Locate every blood parasite and identify its species.
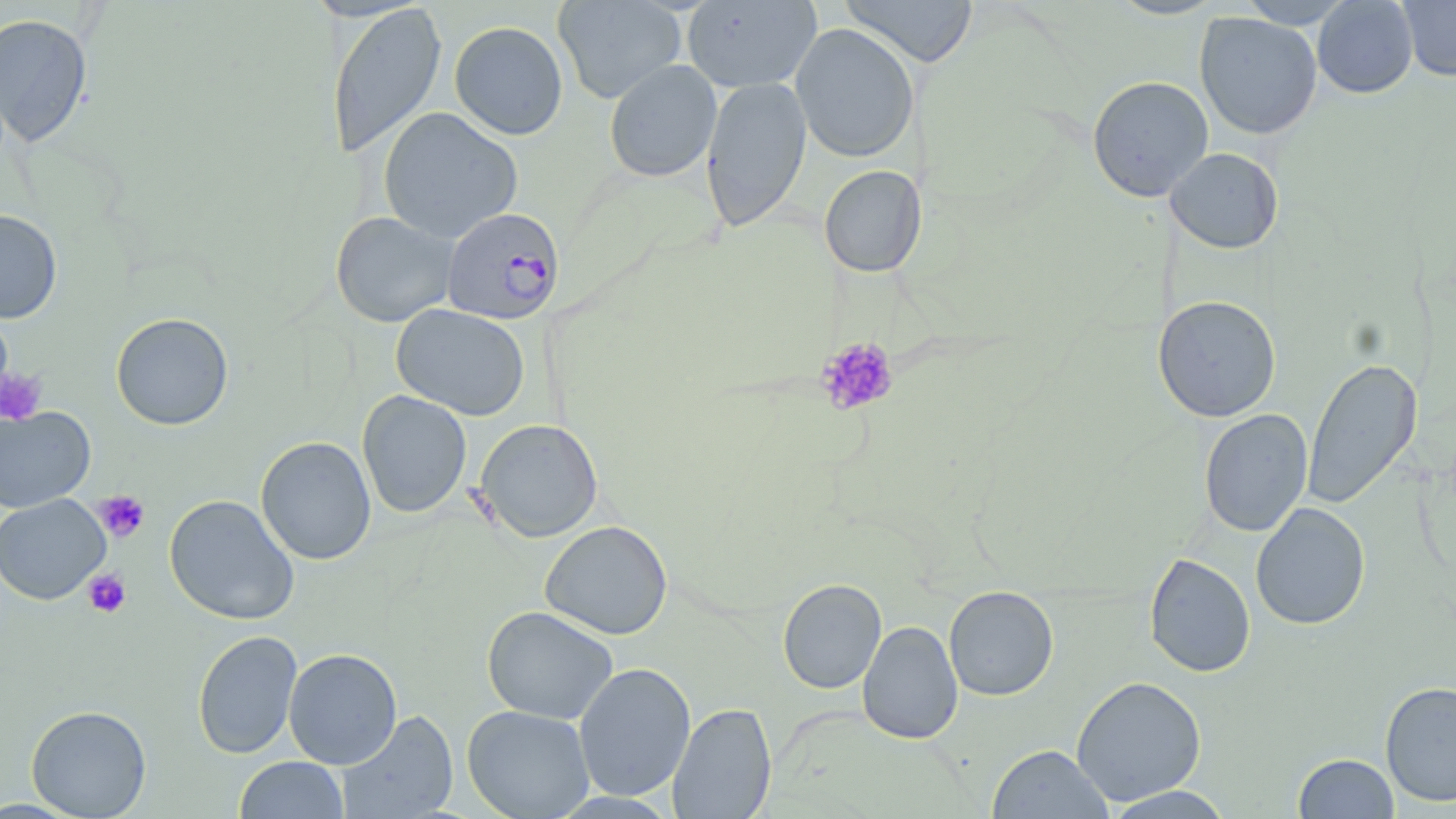

Approximate bounding boxes as [x1, y1, x2, y2] in pixels.
Plasmodium falciparum-infected red blood cells: [443, 206, 565, 325].
No Plasmodium ovale, Plasmodium malariae, Plasmodium vivax, Babesia divergens, or Trypanosoma brucei observed.

Summary:
  - Platelet locations: [816, 337, 899, 416], [0, 367, 47, 426], [94, 491, 149, 543], [82, 568, 131, 618]
  - Uninfected red blood cell locations: [552, 0, 686, 104], [840, 0, 978, 68], [1107, 0, 1226, 20], [1237, 0, 1353, 28], [1313, 0, 1418, 98], [1398, 0, 1456, 81], [682, 1, 821, 93], [326, 4, 446, 159], [1195, 12, 1322, 140], [0, 13, 93, 148], [449, 21, 568, 140], [790, 24, 919, 163], [604, 60, 722, 183], [1087, 75, 1214, 202], [700, 76, 811, 231], [378, 107, 523, 244], [1166, 147, 1284, 253], [818, 165, 927, 278], [0, 208, 63, 323], [330, 211, 458, 327], [1152, 295, 1281, 421], [391, 304, 530, 421], [111, 312, 234, 430], [1302, 357, 1422, 509], [357, 390, 472, 518], [0, 405, 95, 513], [1198, 409, 1313, 537], [475, 418, 603, 543], [255, 436, 377, 565], [0, 493, 110, 605], [164, 494, 300, 625], [1250, 503, 1370, 630], [539, 520, 673, 640], [1143, 552, 1255, 677], [777, 578, 887, 694], [943, 586, 1059, 701], [482, 605, 618, 725], [857, 620, 963, 744], [192, 629, 303, 760], [283, 648, 402, 769], [573, 662, 696, 801], [1071, 675, 1207, 806], [1380, 680, 1456, 807], [668, 702, 776, 819], [26, 704, 152, 818], [462, 704, 594, 819], [336, 709, 459, 818], [987, 744, 1113, 819], [1293, 753, 1399, 818], [234, 756, 349, 818], [1101, 786, 1236, 818]
  - Slide-level diagnosis: Plasmodium falciparum
  - Field of view: single
  - Image size: 1456×819 pixels
  - Modality: light microscopy
  - Stain: May-Grünwald-Giemsa
  - Preparation: thin blood film
  - Magnification: 1000x